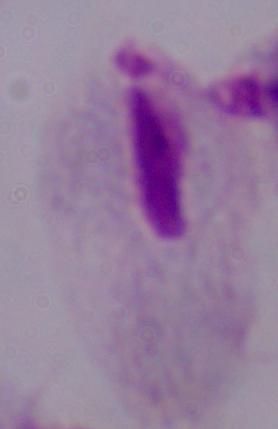
identification = trichomonad
modality = micrograph
magnification = 1000x